Assess the morphology of the red blood cells.
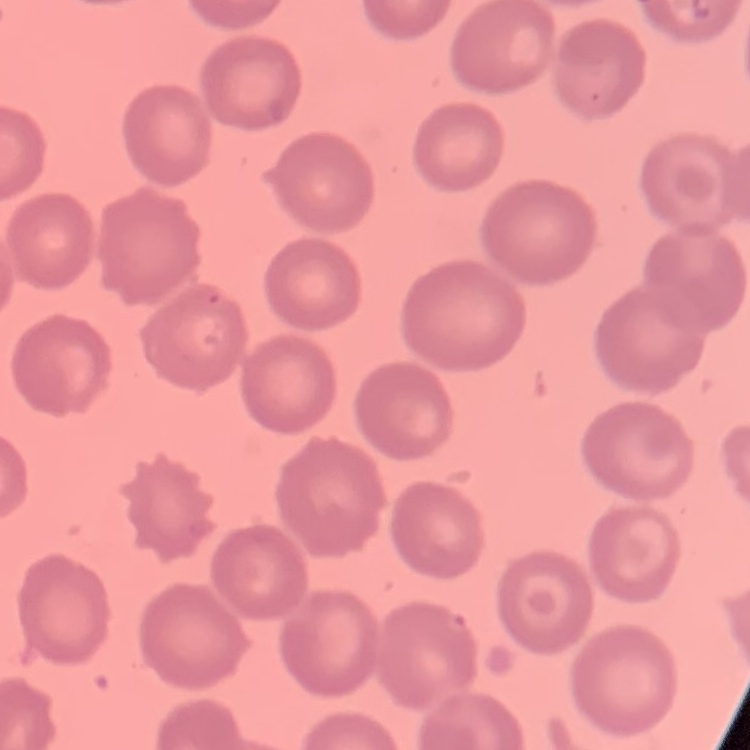

No rouleaux formation.

Square crop of a larger photomicrograph. Thin peripheral smear. Stained with either Field's or Giemsa.